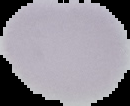

image_size: 130×106 pixels
malaria_status: uninfected
image_type: cell region segmented out of the field of view; surrounding area masked to black
preparation: thin blood smear